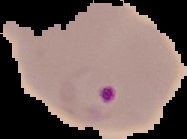

preparation = thin blood film
image size = 187×139 pixels
result = malaria parasites detected
image type = segmented cell region on a black background